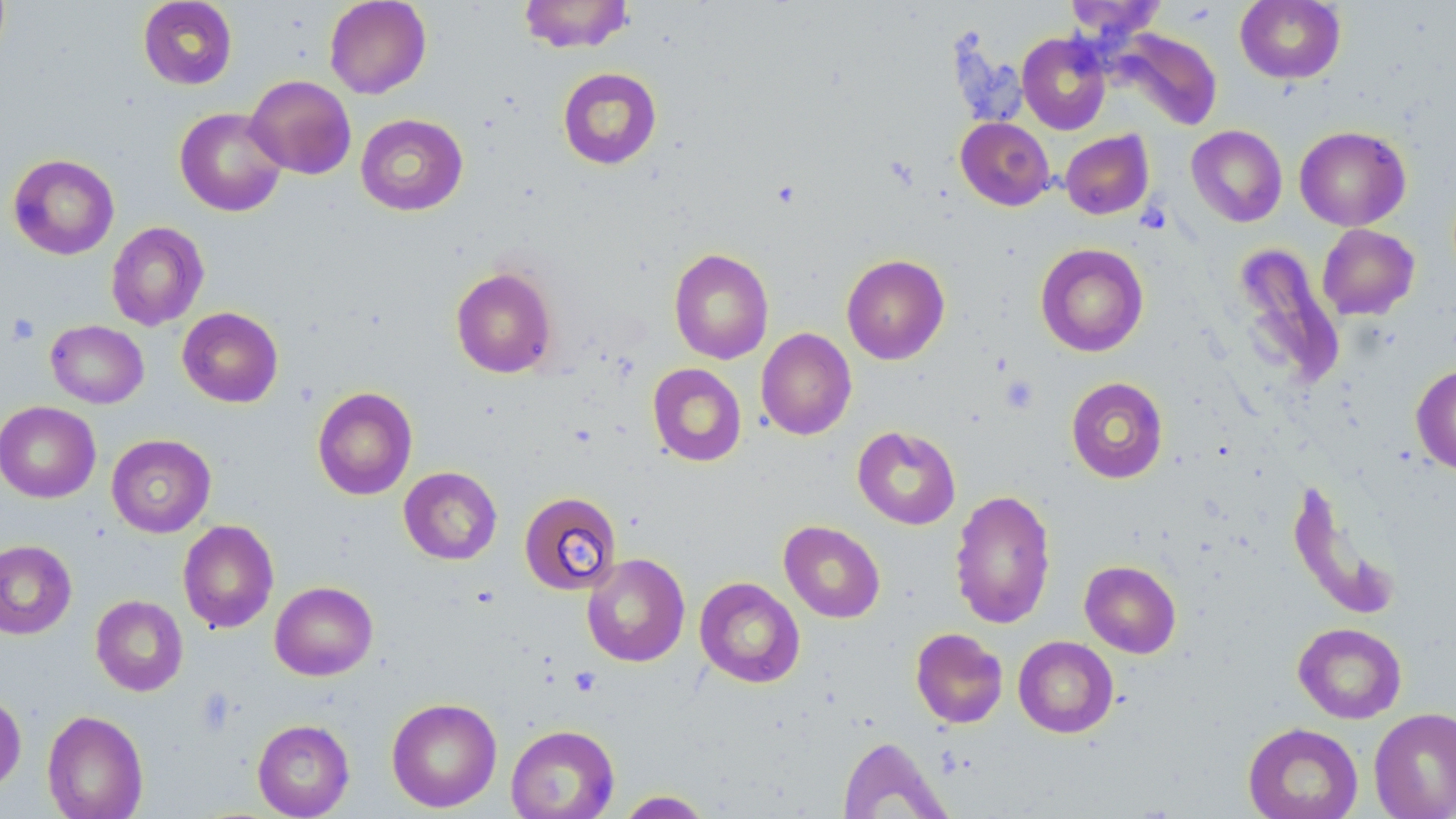
slide-level diagnosis = no evidence of blood parasites
platelet locations = approximate bounding boxes as [x1, y1, x2, y2] in pixels: [7, 314, 41, 346], [1000, 376, 1039, 413], [569, 666, 601, 696], [196, 690, 237, 735]
stain = May-Grünwald-Giemsa
preparation = thin blood smear
uninfected red blood cell locations = approximate bounding boxes as [x1, y1, x2, y2] in pixels: [137, 0, 238, 90], [324, 0, 431, 99], [518, 0, 634, 53], [1235, 0, 1346, 84], [1064, 1, 1166, 42], [1112, 28, 1222, 131], [1017, 33, 1111, 135], [557, 67, 662, 170], [245, 75, 356, 179], [174, 107, 287, 216], [355, 114, 468, 216], [955, 117, 1055, 211], [1187, 125, 1287, 227], [1294, 125, 1411, 231], [1060, 130, 1154, 219], [8, 153, 119, 260], [106, 221, 209, 331], [1317, 224, 1420, 320], [1035, 243, 1149, 356], [1232, 243, 1345, 388], [669, 248, 774, 365], [841, 254, 950, 364], [451, 267, 558, 379], [177, 307, 283, 407], [46, 320, 149, 408], [755, 328, 857, 440], [647, 363, 747, 467], [1411, 364, 1456, 475], [1066, 377, 1168, 483], [312, 386, 418, 500], [0, 401, 100, 503], [852, 425, 961, 529], [106, 434, 216, 537], [399, 466, 502, 564], [1287, 478, 1403, 619], [949, 488, 1056, 630], [519, 491, 622, 595], [178, 519, 278, 633], [779, 520, 886, 623], [0, 540, 76, 639], [582, 552, 690, 667], [1079, 560, 1182, 658], [694, 577, 805, 688], [270, 581, 378, 681], [91, 595, 188, 696], [1293, 622, 1407, 723], [911, 628, 1008, 728], [1013, 636, 1118, 738], [0, 690, 26, 793], [386, 697, 502, 812], [1369, 706, 1456, 819], [42, 710, 149, 819], [252, 719, 355, 818], [1243, 723, 1363, 819], [505, 724, 620, 819], [837, 736, 951, 819], [615, 790, 714, 818]
image size = 1456×819 pixels
field of view = one of a larger specimen
magnification = 1000x
modality = light microscopy